Identify the blood parasite species.
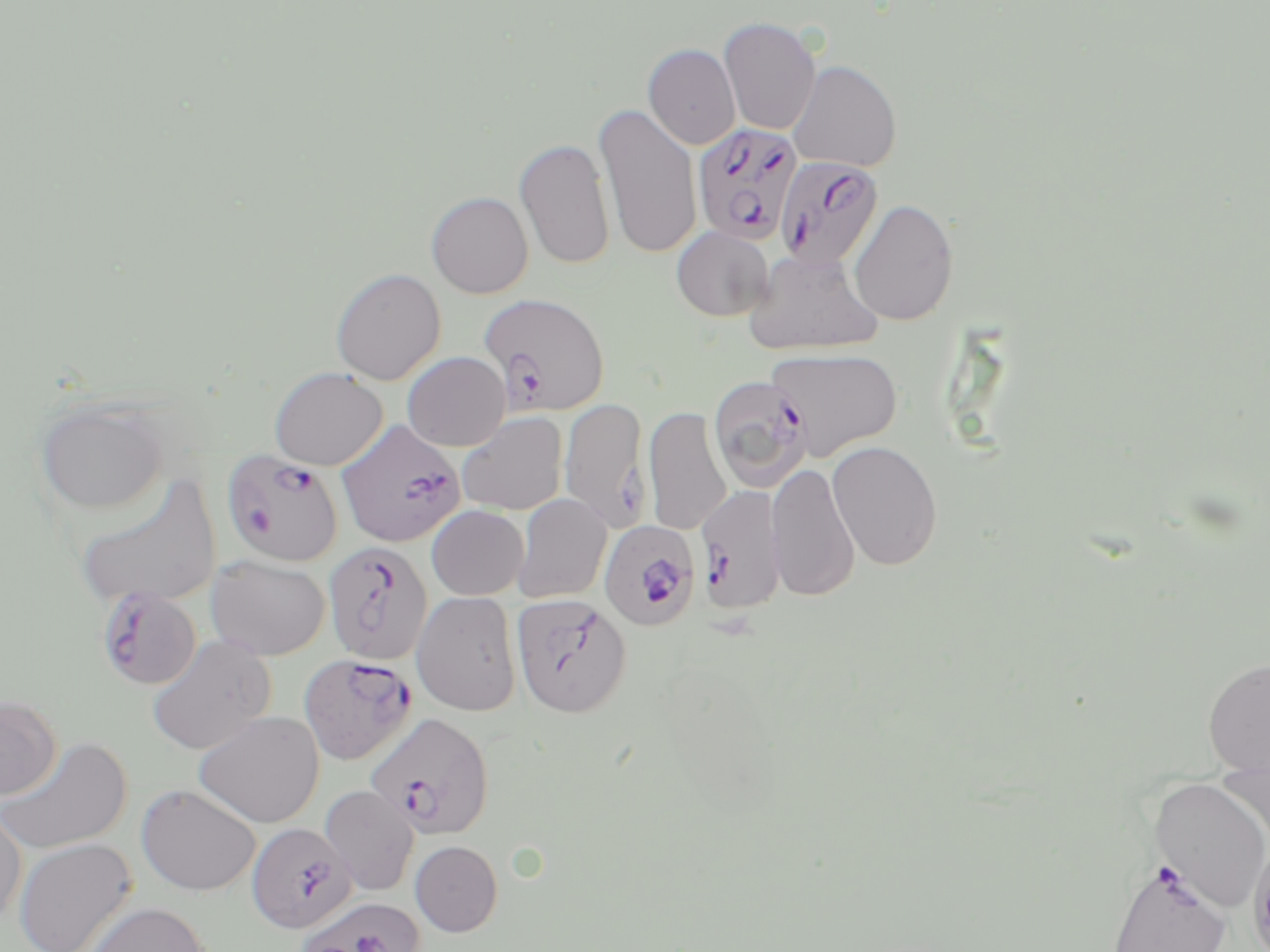

Plasmodium falciparum.

Approximate bounding boxes as (x1, y1, x2, y2) in pixels. Plasmodium falciparum-infected red blood cell locations (subset): (692, 122, 804, 245), (775, 155, 884, 270), (481, 295, 611, 420), (708, 375, 812, 492), (336, 420, 465, 548), (223, 451, 345, 568), (695, 485, 786, 613), (599, 520, 700, 629), (324, 541, 433, 664), (95, 585, 202, 690), (299, 653, 416, 765), (365, 713, 494, 839), (246, 822, 356, 933), (297, 897, 429, 952). Platelet locations: (245, 507, 275, 535). Uninfected red blood cell locations (subset): (719, 17, 822, 135), (643, 43, 741, 150), (787, 60, 902, 172), (594, 102, 703, 260), (515, 137, 615, 269), (426, 191, 533, 299), (848, 198, 959, 326), (672, 227, 773, 321), (743, 247, 883, 356), (330, 268, 446, 385), (765, 348, 902, 460), (402, 352, 510, 451), (269, 367, 388, 470), (33, 396, 170, 517), (559, 397, 651, 530), (643, 406, 731, 536), (457, 412, 568, 515), (827, 440, 943, 570), (766, 461, 860, 602), (73, 474, 222, 609), (512, 494, 612, 603), (426, 505, 529, 600), (207, 555, 330, 660), (411, 590, 522, 716), (146, 633, 276, 756), (1203, 657, 1270, 775), (0, 695, 62, 801), (194, 711, 325, 828), (0, 736, 133, 856), (1149, 777, 1270, 912), (136, 784, 261, 896), (320, 785, 419, 895), (0, 804, 27, 926), (13, 838, 137, 952), (410, 840, 503, 937), (1106, 857, 1233, 952), (81, 902, 212, 952). May-Grünwald-Giemsa-stained preparation. Image is 1270×952 pixels. Thin blood film. Single field of view. Optical microscopy. 1000x magnification.